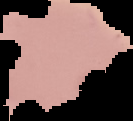 Image is 133×121 pixels. The area outside the segmented cell region is set to black. From a thin blood film. Result: no Plasmodium parasites detected.